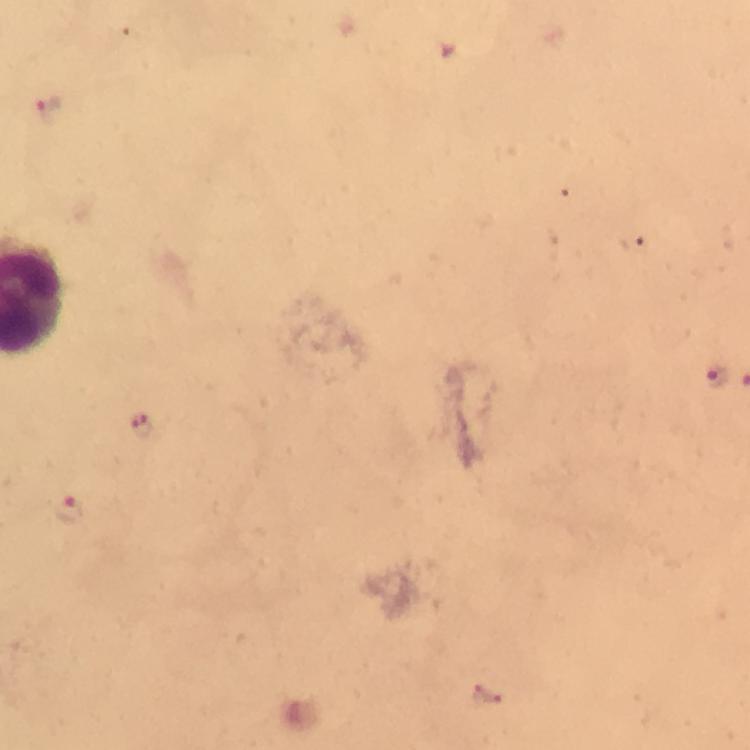
magnification = 100x
immersion oil = applied
malaria parasite locations = approximate object centers, in pixels from the top-left corner: (x=48, y=111), (x=716, y=374), (x=139, y=426), (x=68, y=510)
image size = 750×750 pixels
stain = Giemsa
context = from a diagnostic examination for malaria
preparation = thick blood film
cropped from = one field of view
capture = smartphone photograph through a microscope